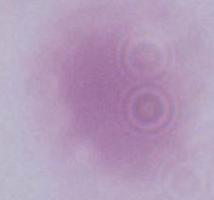 Micrograph. A red blood cell is shown. Captured at 1000x magnification.